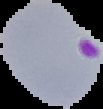 From a thin blood smear. Image is 103×109 pixels. The area outside the segmented cell region is set to black. Malaria status: parasitized.